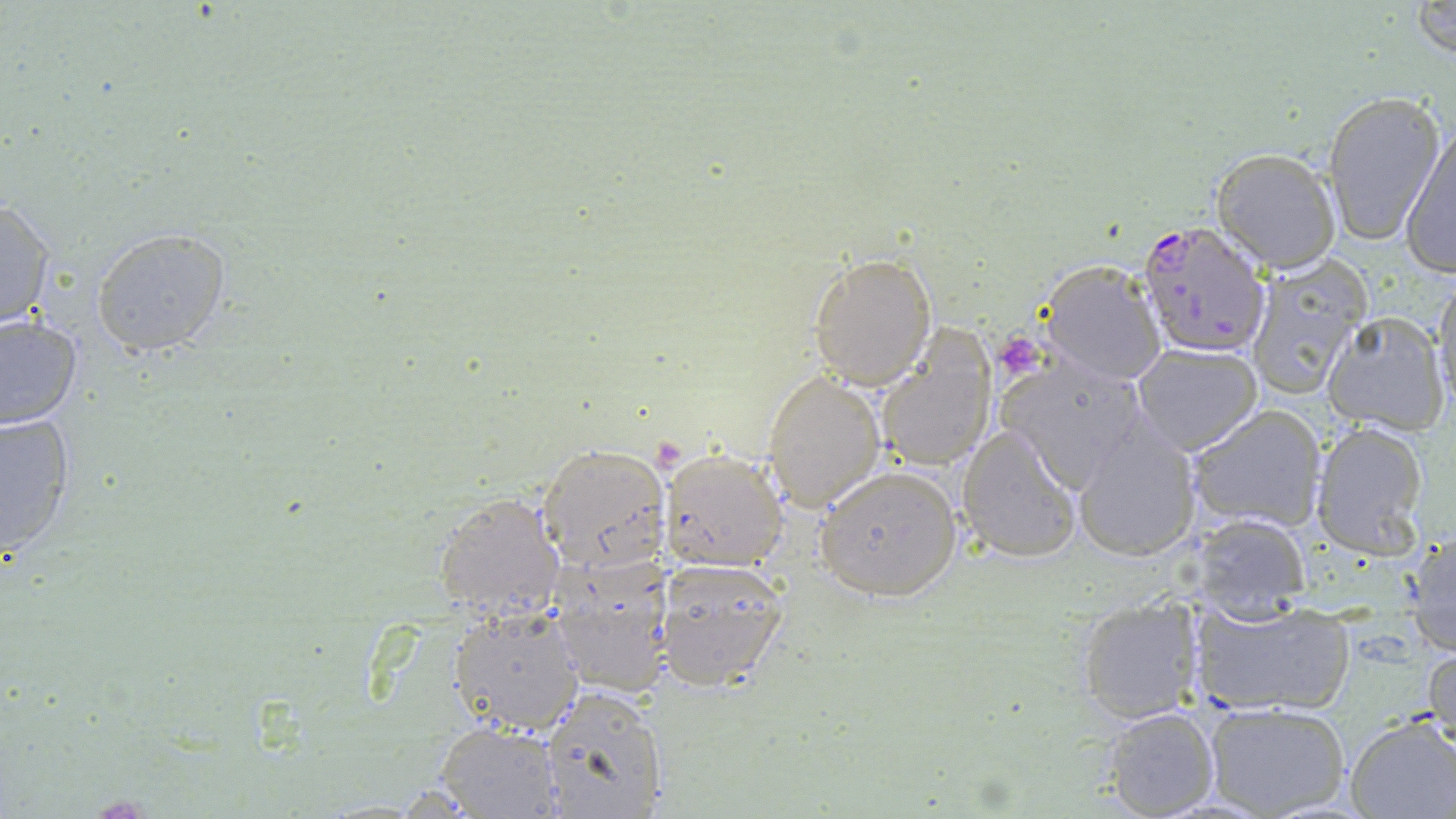
Approximate bounding boxes as (x1, y1, x2, y2) in pixels. Plasmodium falciparum-infected red blood cell locations: (1135, 218, 1276, 361). Uninfected red blood cell locations: (1411, 0, 1455, 60), (1320, 89, 1444, 245), (1399, 122, 1455, 279), (1210, 147, 1342, 274), (0, 197, 56, 329), (92, 228, 231, 357), (807, 252, 938, 389), (1243, 253, 1371, 402), (1037, 258, 1167, 386), (1432, 276, 1456, 417), (1320, 312, 1450, 433), (0, 316, 83, 430), (878, 337, 995, 471), (1129, 342, 1262, 456), (1002, 356, 1156, 493), (762, 370, 887, 511), (1187, 404, 1327, 534), (0, 412, 76, 559), (1311, 421, 1431, 558), (955, 422, 1082, 564), (1071, 425, 1201, 563), (539, 443, 668, 569), (658, 447, 787, 571), (817, 466, 962, 601), (433, 490, 566, 621), (1182, 509, 1313, 618), (1404, 526, 1456, 657), (547, 555, 673, 697), (654, 557, 788, 691), (1076, 596, 1207, 722), (1187, 597, 1356, 717), (446, 607, 587, 736), (1426, 641, 1456, 761), (539, 688, 669, 818), (1201, 700, 1351, 818), (1101, 706, 1221, 818), (1344, 717, 1456, 819), (436, 721, 565, 817). Platelet locations: (996, 329, 1040, 375). Slide-level diagnosis: Plasmodium falciparum. Image is 1456×819 pixels. Light microscopy. 1000x magnification. One field of a larger specimen. Thin blood smear. May-Grünwald-Giemsa stain.